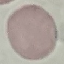

Result: no malaria parasites seen. Thin blood smear. Giemsa stain. Cell patch, automatically extracted from a larger field of view and resized to 64 × 64 pixels. Acquired by smartphone through the microscope eyepiece.